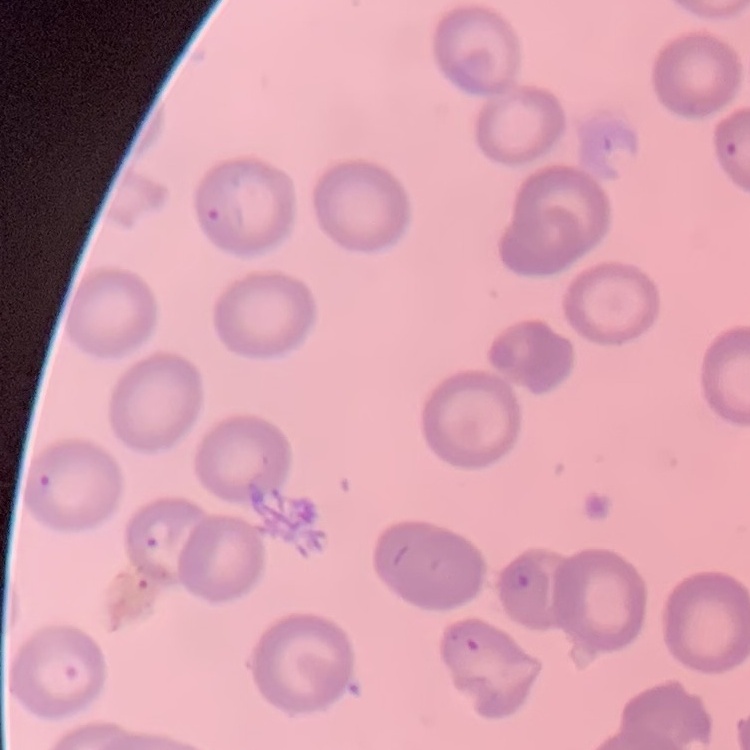 The erythrocytes show no rouleaux formation. Thin peripheral smear. Field's or Giemsa stain. One tile cut from a larger photomicrograph.